Describe the morphology of the erythrocytes.
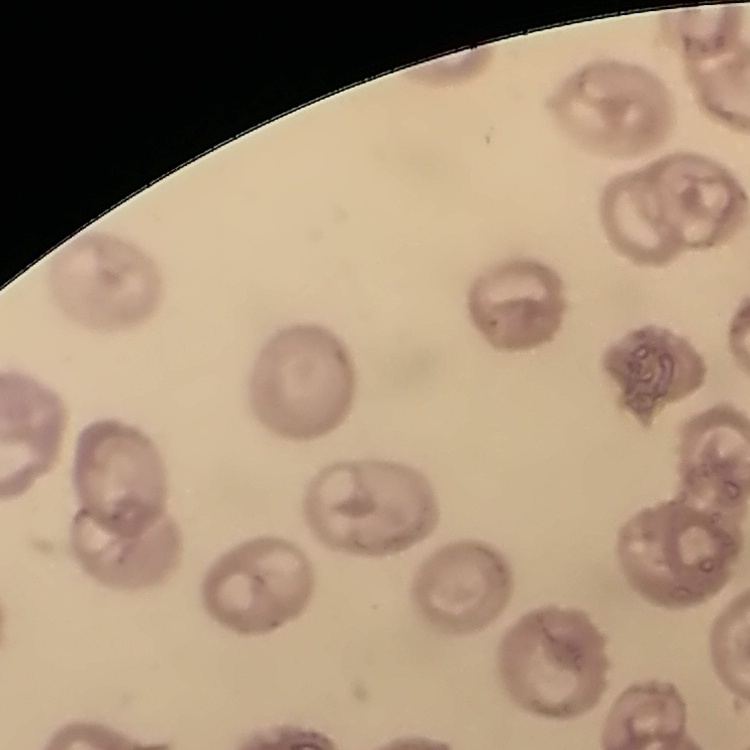

They show no rouleaux formation.

Summary:
  - Stain: Field's or Giemsa
  - Preparation: thin blood smear
  - Image type: one tile cut from a larger photomicrograph